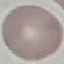
Result: negative for malaria parasites. Thin smear of blood. Photographed with a smartphone camera at the microscope eyepiece. Giemsa stain. Cell patch, automatically extracted from a larger field of view and resized to 64 × 64 pixels.